Outline each uninfected red blood cell.
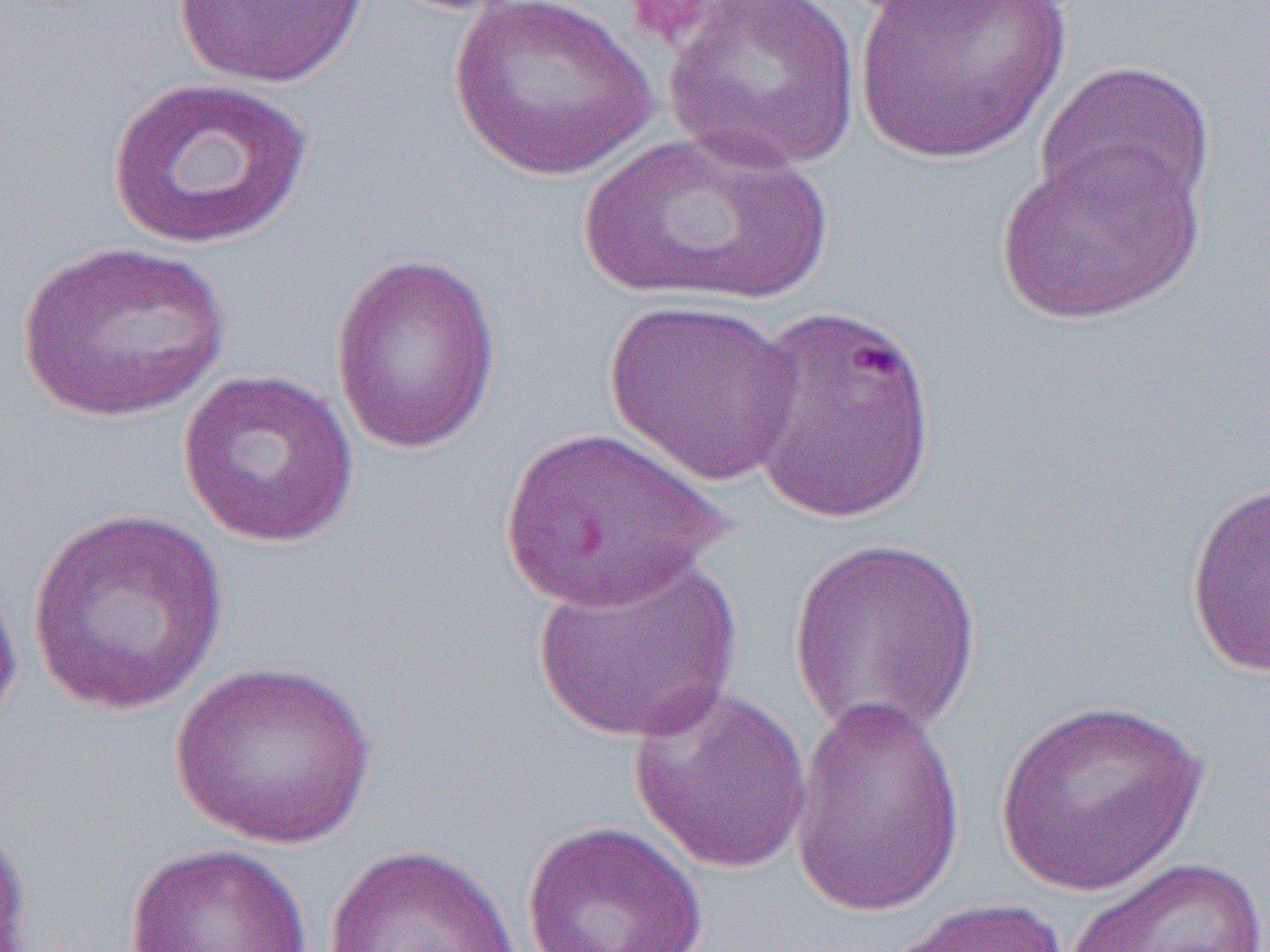

Approximate bounding boxes as named x1/y1/x2/y2 corners in pixels.
Uninfected red blood cells: (x1=449, y1=0, x2=657, y2=180), (x1=663, y1=0, x2=862, y2=175), (x1=849, y1=0, x2=1071, y2=166), (x1=172, y1=1, x2=370, y2=88), (x1=1034, y1=59, x2=1216, y2=225), (x1=106, y1=76, x2=314, y2=251), (x1=571, y1=129, x2=833, y2=308), (x1=996, y1=143, x2=1205, y2=326), (x1=16, y1=240, x2=231, y2=422), (x1=329, y1=252, x2=502, y2=456), (x1=602, y1=299, x2=803, y2=487), (x1=738, y1=301, x2=939, y2=523), (x1=177, y1=367, x2=361, y2=549), (x1=500, y1=424, x2=728, y2=612), (x1=1184, y1=478, x2=1270, y2=679), (x1=26, y1=508, x2=230, y2=717), (x1=786, y1=536, x2=984, y2=743), (x1=531, y1=552, x2=745, y2=744), (x1=0, y1=557, x2=25, y2=745), (x1=169, y1=658, x2=377, y2=850), (x1=628, y1=685, x2=815, y2=875), (x1=788, y1=695, x2=966, y2=918), (x1=992, y1=696, x2=1211, y2=897), (x1=0, y1=817, x2=32, y2=952), (x1=521, y1=819, x2=709, y2=952), (x1=122, y1=842, x2=314, y2=951), (x1=322, y1=843, x2=522, y2=952), (x1=1063, y1=856, x2=1270, y2=952), (x1=879, y1=897, x2=1075, y2=952).

slide-level diagnosis = Plasmodium falciparum
preparation = thin blood film
image size = 1270×952 pixels
magnification = 1000x
field of view = single
modality = light microscopy
platelet locations = approximate bounding boxes as named x1/y1/x2/y2 corners in pixels: (x1=619, y1=0, x2=725, y2=49)